Classify this cell by malaria status.
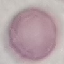

It is uninfected.

Summary:
  - Stain: Giemsa
  - Preparation: thin blood smear
  - Capture: smartphone camera at the microscope eyepiece
  - Image type: automatically extracted cell patch, resized to 64 × 64 pixels